Name the parasite shown.
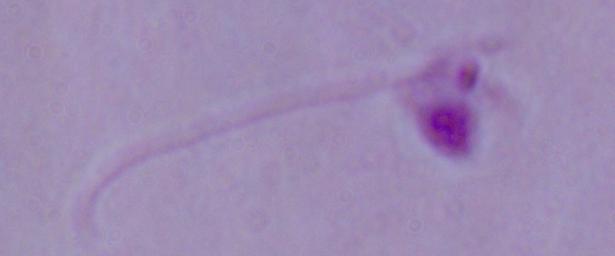

Leishmania.

magnification = 1000x
modality = photomicrograph